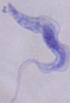
1000x magnification. Photomicrograph. A trypanosome is shown.